Comment on the morphology of the red blood cells.
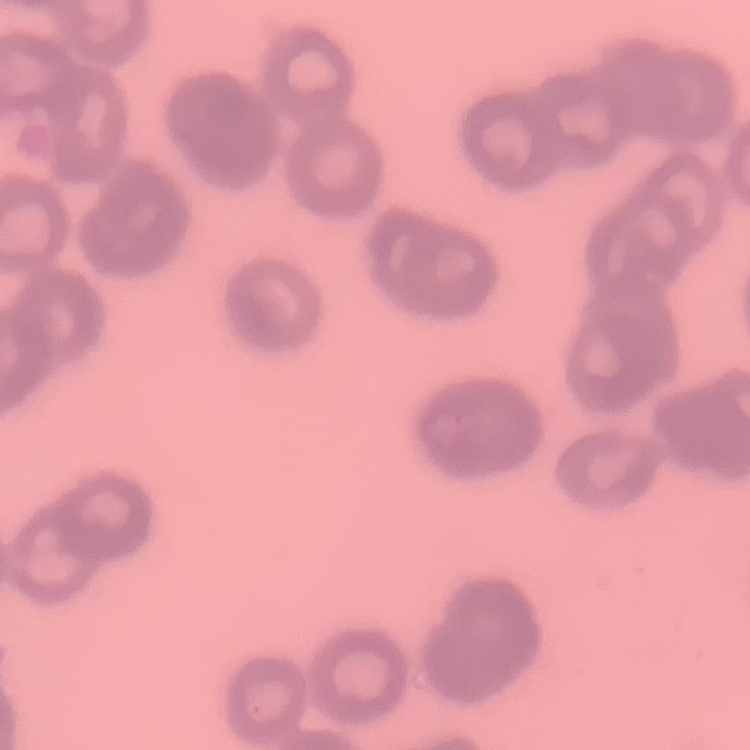
Rouleaux formation.

stain = Field's or Giemsa
preparation = thin peripheral smear
image type = square crop of a larger photomicrograph